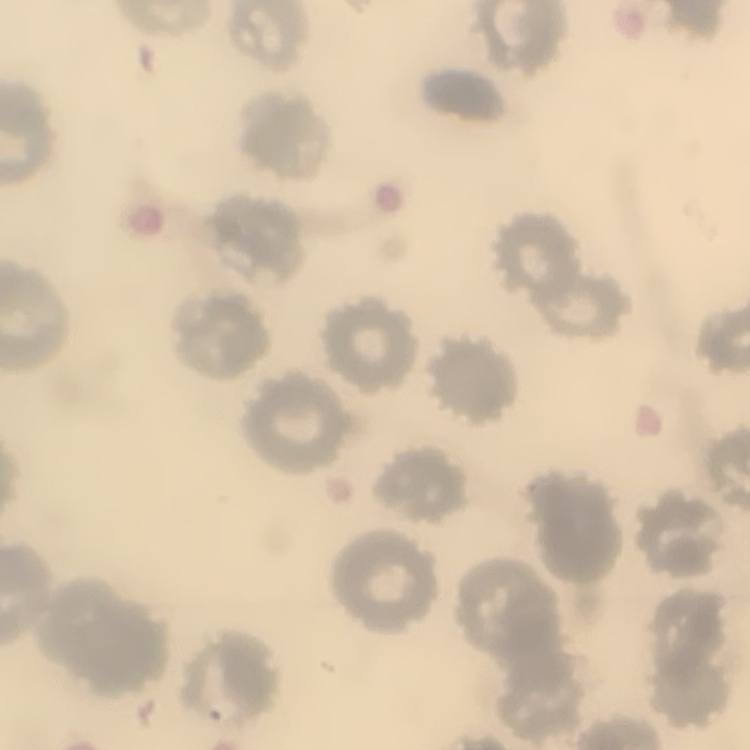

The erythrocytes exhibit no rouleaux formation. Field's or Giemsa stain. Thin blood smear. Square crop of a larger photomicrograph.